Give the position of every malaria parasite.
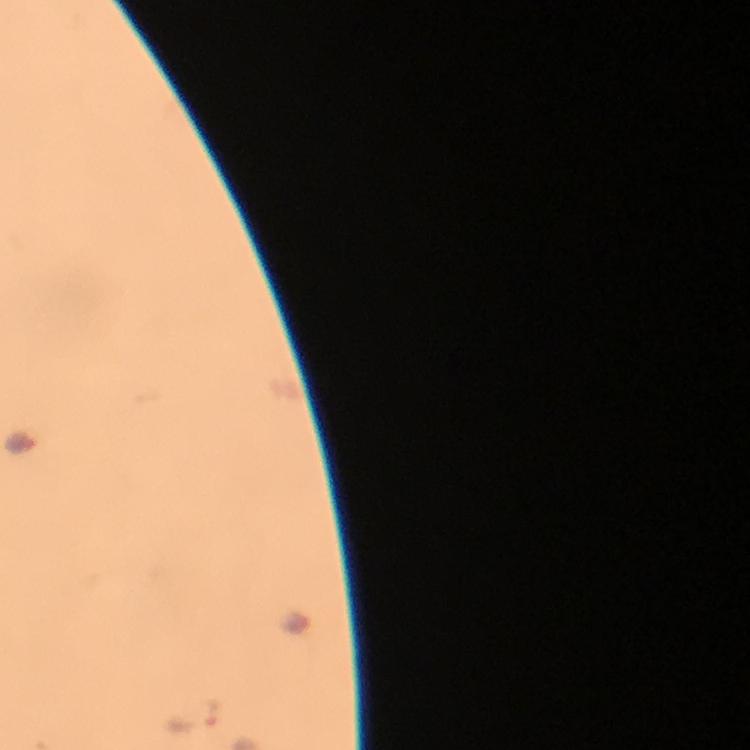
Approximate object centers, in pixels from the top-left corner.
Malaria parasites: (x=193, y=715).

Thick blood film. Smartphone photograph taken through a microscope. Giemsa stain. At 100x magnification. A crop from one field of view. Immersion oil was used. From a malaria diagnostic workup. Image is 750×750 pixels.